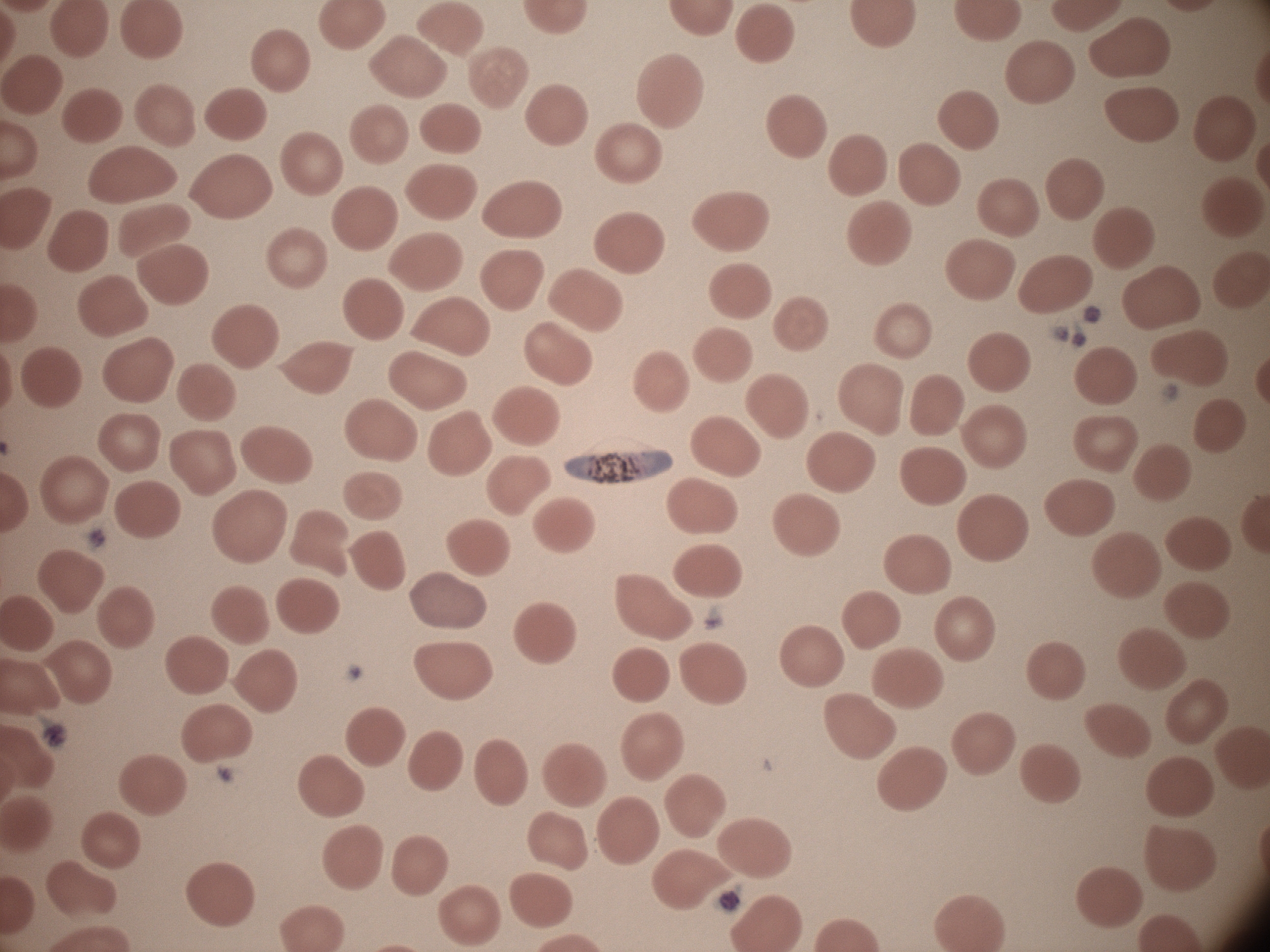

Approximate bounding boxes as named x1/y1/x2/y2 corners in pixels, from the source annotation, which is not necessarily exhaustive.
Summary:
  - Gametocyte locations: (x1=563, y1=449, x2=673, y2=486)
  - Image size: 1270×952 pixels
  - Field of view: one from this slide
  - Stain: Giemsa
  - Microscope: Leica DM2000 with built-in camera
  - Preparation: thin blood smear
  - Species: Plasmodium falciparum
  - Magnification: 100x